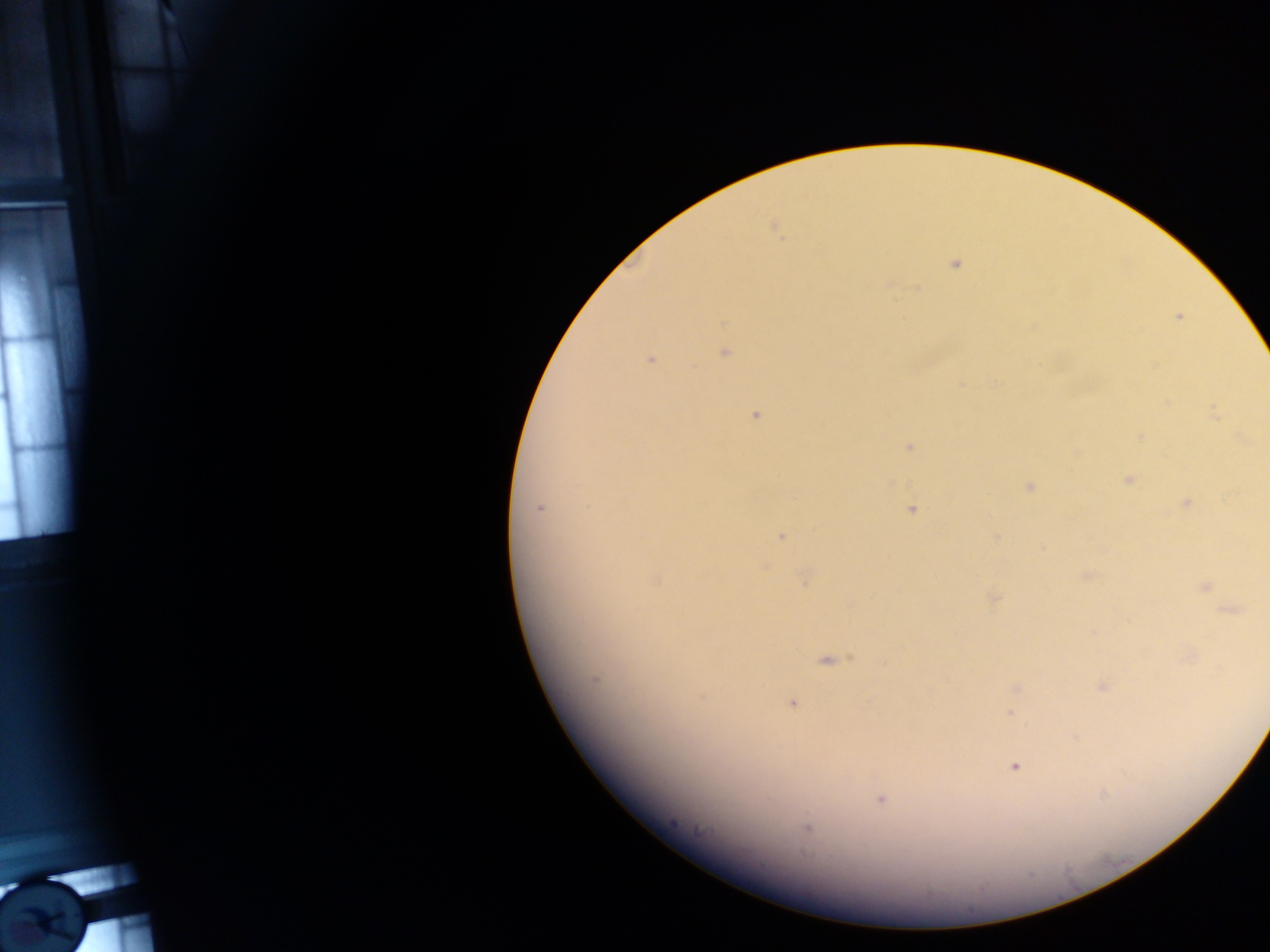

Approximate centers as [x, y] in pixels.
Summary:
  - Plasmodium parasite locations: [777, 230], [955, 264], [1178, 317], [725, 352], [651, 359], [1214, 412], [756, 414], [1139, 435], [1242, 438], [909, 447], [1129, 480], [1028, 486], [1186, 502], [539, 508], [912, 510], [782, 536], [995, 539], [1086, 575], [805, 579], [655, 580], [1204, 586], [993, 598], [1231, 611], [1092, 632], [826, 660], [595, 680], [1102, 686], [1016, 688], [702, 697], [792, 703], [1010, 714], [1075, 737], [1014, 766], [880, 799], [807, 828]
  - Leukocyte locations: [46, 911]
  - Capture: mobile-phone photograph through a microscope
  - Image size: 1270×952 pixels
  - Country: Ghana
  - Field of view: single
  - Preparation: thick blood smear